Locate platelets.
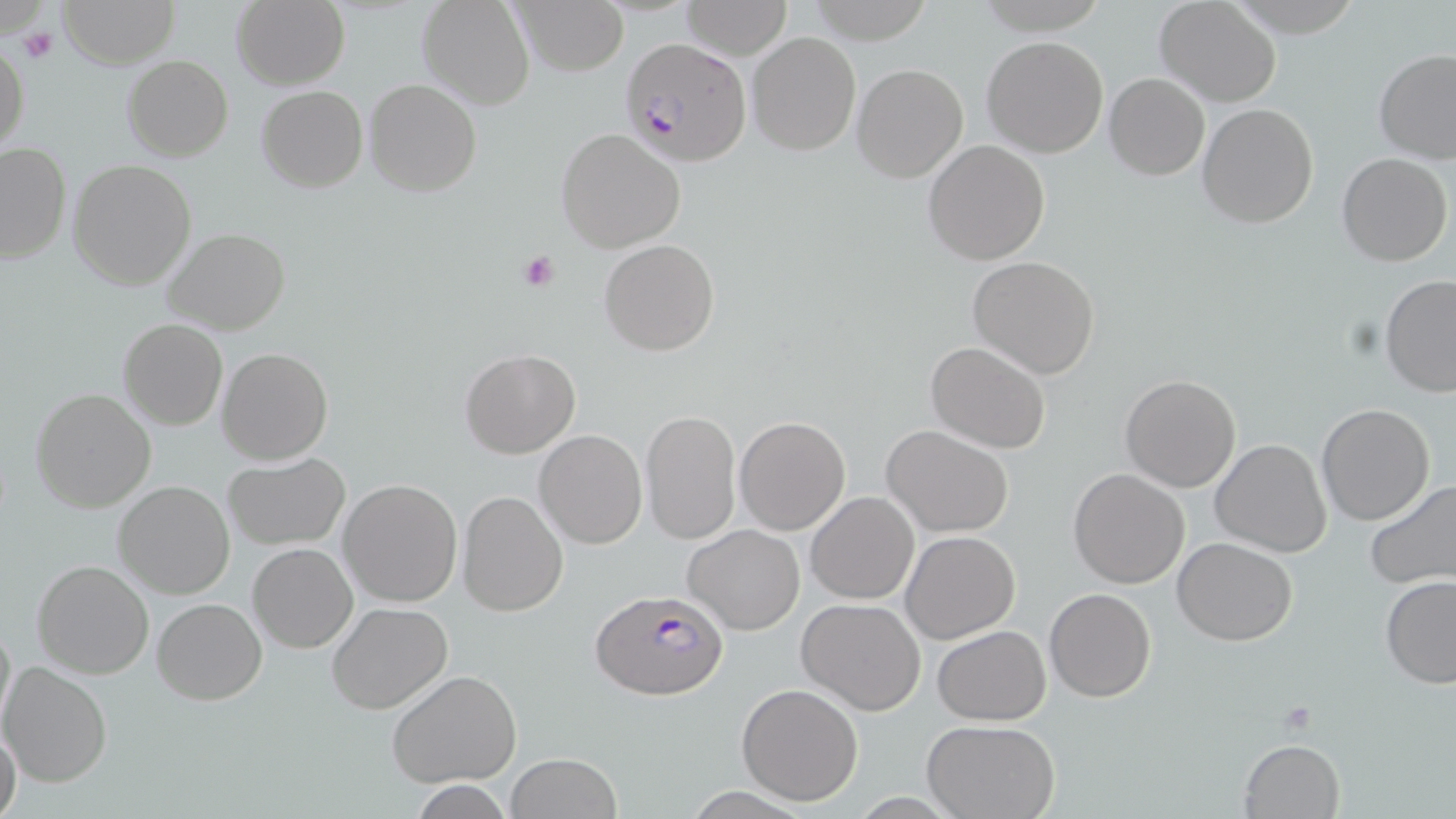

Approximate bounding boxes as [x1, y1, x2, y2] in pixels.
Platelets: [18, 24, 58, 65], [517, 249, 561, 292], [1277, 700, 1317, 732].

Plasmodium falciparum-infected red blood cell locations = approximate bounding boxes as [x1, y1, x2, y2] in pixels: [619, 36, 753, 167], [589, 589, 728, 702]
slide-level diagnosis = Plasmodium falciparum
image size = 1456×819 pixels
field of view = one of a larger specimen
preparation = thin blood film
stain = May-Grünwald-Giemsa
uninfected red blood cell locations = approximate bounding boxes as [x1, y1, x2, y2] in pixels: [58, 0, 179, 68], [232, 0, 349, 89], [417, 0, 534, 110], [509, 0, 629, 75], [802, 0, 935, 43], [680, 1, 792, 60], [1155, 1, 1281, 106], [748, 31, 861, 156], [982, 36, 1108, 157], [0, 41, 28, 153], [1373, 49, 1456, 164], [123, 55, 232, 161], [851, 62, 969, 183], [1104, 73, 1210, 180], [365, 79, 482, 199], [257, 84, 367, 193], [1197, 102, 1320, 229], [556, 128, 686, 252], [923, 139, 1050, 265], [0, 143, 71, 264], [1336, 153, 1452, 267], [68, 159, 196, 290], [162, 227, 290, 334], [598, 238, 719, 356], [967, 256, 1100, 378], [1379, 273, 1456, 400], [118, 320, 229, 431], [925, 340, 1053, 454], [217, 347, 334, 465], [460, 349, 579, 458], [1120, 374, 1241, 493], [30, 387, 158, 514], [1317, 403, 1435, 526], [641, 409, 740, 544], [734, 416, 851, 535], [882, 425, 1014, 537], [535, 430, 646, 549], [1211, 437, 1332, 557], [223, 453, 350, 550], [1068, 467, 1189, 588], [337, 478, 463, 608], [1365, 479, 1456, 588], [114, 481, 236, 599], [459, 490, 569, 617], [806, 491, 919, 604], [683, 525, 804, 634], [900, 531, 1019, 643], [1171, 537, 1300, 644], [247, 542, 357, 653], [32, 560, 156, 679], [1380, 575, 1456, 689], [1044, 588, 1155, 702], [154, 599, 267, 704], [796, 599, 926, 716], [326, 601, 453, 714], [0, 614, 15, 738], [932, 624, 1051, 726], [0, 661, 115, 787], [388, 671, 522, 787], [736, 683, 864, 805], [922, 719, 1063, 818], [0, 723, 23, 819], [1238, 737, 1345, 819], [505, 752, 623, 819], [410, 782, 517, 818]
modality = light microscopy
magnification = 1000x